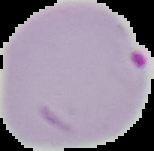
image size = 154×151 pixels
preparation = thin blood film
result = Plasmodium parasites detected
image type = segmented cell region with the area outside set to black